Identify the parasite.
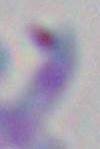
This is Toxoplasma gondii.

{
  "magnification": "1000x",
  "modality": "micrograph"
}